Identify the parasite.
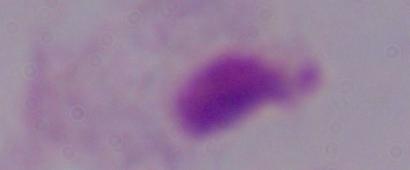

A trichomonad.

Summary:
  - Magnification: 1000x
  - Modality: micrograph